Assess this cell for malaria.
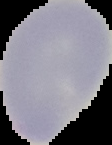
Uninfected.

Image is 112×145 pixels. The area outside the segmented cell region is set to black. From a thin blood film.